Name the blood parasite species.
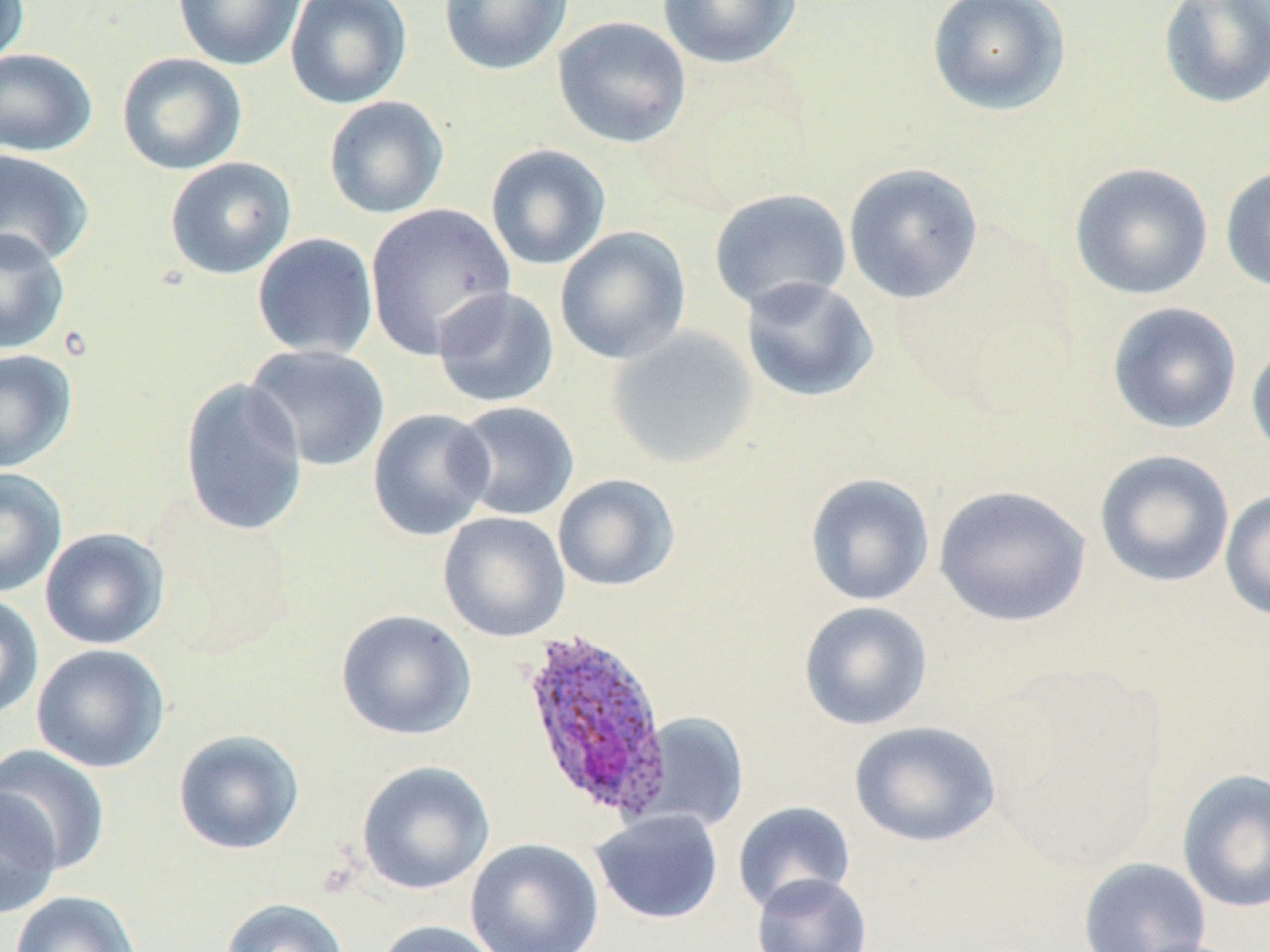

Plasmodium ovale.

Summary:
  - Coordinate format: approximate bounding boxes as (x1, y1, x2, y2) in pixels
  - Plasmodium ovale-infected red blood cell locations: (518, 626, 674, 821)
  - Uninfected red blood cell locations: (0, 0, 31, 68), (172, 0, 306, 71), (285, 0, 412, 109), (438, 0, 573, 76), (656, 0, 803, 69), (926, 0, 1071, 116), (1158, 0, 1270, 109), (552, 16, 693, 149), (0, 48, 98, 157), (116, 52, 248, 175), (323, 96, 449, 219), (485, 143, 611, 270), (0, 148, 95, 268), (164, 156, 297, 280), (843, 162, 984, 304), (1069, 162, 1214, 300), (1219, 163, 1270, 294), (709, 187, 852, 314), (364, 203, 516, 359), (554, 226, 692, 365), (0, 228, 71, 355), (250, 232, 379, 360), (739, 275, 879, 403), (432, 286, 560, 409), (1107, 302, 1242, 435), (605, 327, 759, 469), (1246, 334, 1270, 463), (244, 343, 390, 473), (0, 349, 78, 473), (178, 377, 309, 536), (450, 401, 580, 522), (367, 408, 495, 541), (1094, 449, 1235, 588), (0, 468, 67, 599), (804, 472, 935, 607), (552, 474, 681, 592), (933, 484, 1092, 628), (1220, 489, 1270, 623), (438, 511, 570, 642), (39, 527, 170, 650), (0, 592, 44, 722), (798, 601, 933, 731), (335, 609, 477, 741), (31, 643, 170, 774), (636, 714, 750, 833), (850, 720, 1000, 848), (172, 728, 305, 856), (0, 743, 111, 876), (356, 760, 496, 896), (1176, 768, 1270, 914), (0, 787, 61, 921), (732, 801, 855, 915), (590, 809, 724, 925), (465, 838, 604, 952), (1077, 857, 1212, 952), (751, 872, 873, 952), (9, 891, 142, 952), (219, 897, 351, 952), (374, 920, 503, 952)
  - Magnification: 1000x
  - Stain: May-Grünwald-Giemsa
  - Image size: 1270×952 pixels
  - Field of view: one of a larger specimen
  - Preparation: thin blood film
  - Modality: light microscopy